Report the malaria status of this cell.
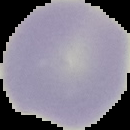

It is uninfected.

preparation = thin blood film
image size = 130×130 pixels
image type = segmented cell region on a black background